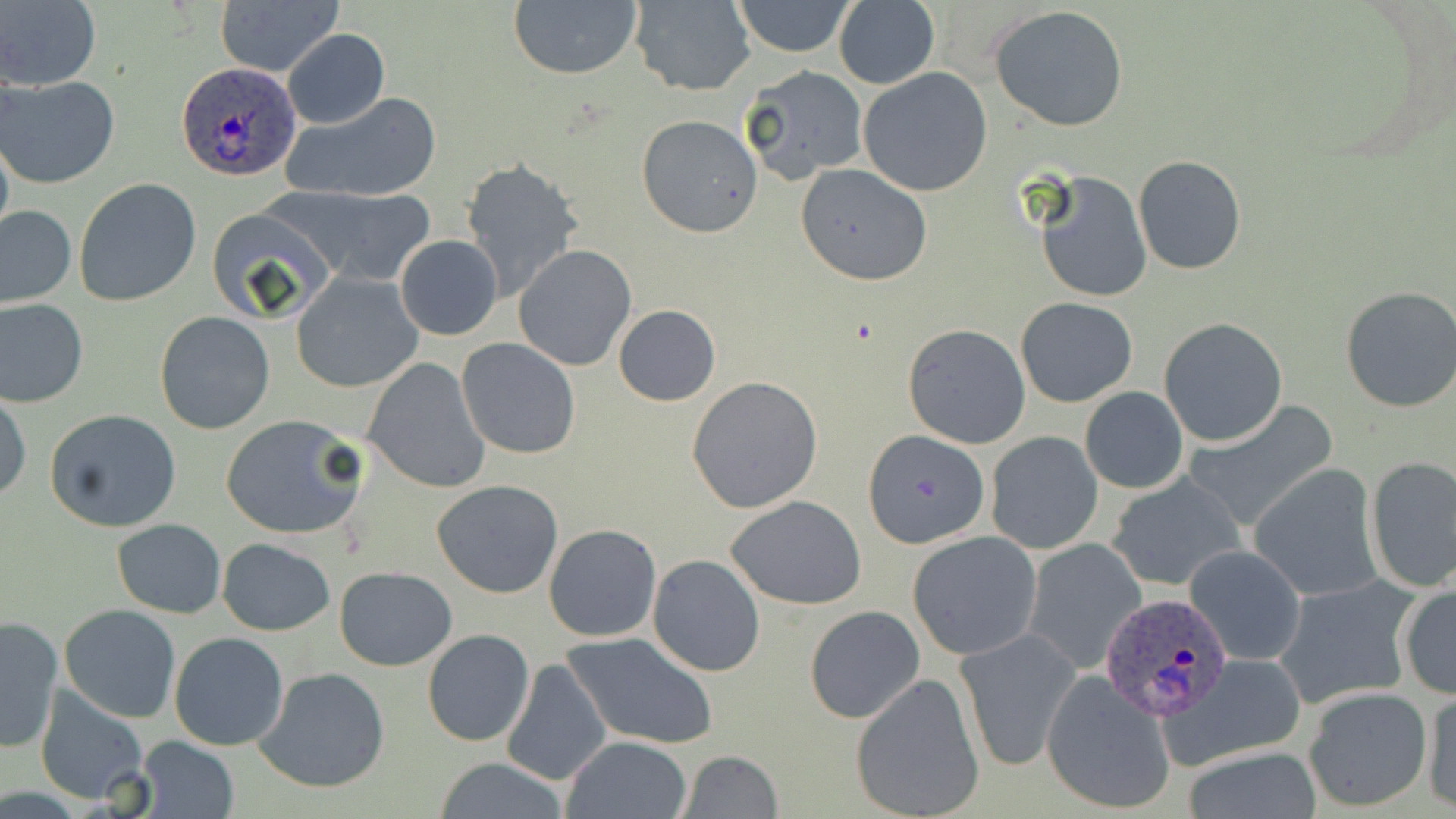
Summary:
  - Coordinate format: approximate bounding boxes as (x1,y1)-(x2,y2) corner pairs in pixels
  - Plasmodium ovale-infected red blood cell locations: (177,62)-(302,181), (1096,592)-(1232,720)
  - Uninfected red blood cell locations: (216,0)-(343,78), (507,0)-(643,81), (732,0)-(857,57), (1,1)-(101,91), (627,1)-(755,95), (834,2)-(940,88), (990,5)-(1129,131), (284,29)-(389,129), (741,64)-(870,183), (859,68)-(993,196), (2,74)-(122,188), (279,91)-(441,204), (636,116)-(763,238), (1133,155)-(1246,274), (460,159)-(583,300), (795,162)-(932,285), (1035,170)-(1152,304), (74,179)-(202,305), (283,187)-(435,285), (0,205)-(76,308), (207,207)-(340,326), (395,235)-(504,340), (514,246)-(636,371), (291,272)-(423,393), (1338,285)-(1456,414), (1015,296)-(1138,408), (0,297)-(88,408), (612,305)-(721,406), (153,311)-(275,435), (1159,317)-(1289,447), (902,323)-(1031,449), (456,338)-(581,459), (361,357)-(491,494), (686,375)-(823,513), (1081,386)-(1188,494), (0,391)-(30,506), (1184,403)-(1338,532), (46,409)-(184,533), (220,413)-(367,539), (863,431)-(989,547), (986,432)-(1102,554), (1364,455)-(1456,594), (1249,464)-(1383,603), (1105,471)-(1245,593), (430,479)-(564,599), (726,495)-(867,607), (112,519)-(225,618), (543,524)-(663,643), (906,531)-(1042,659), (217,537)-(336,635), (1021,538)-(1146,674), (1185,545)-(1306,666), (648,554)-(765,677), (333,566)-(456,670), (1271,576)-(1420,710), (1397,580)-(1456,701), (59,604)-(181,723), (804,605)-(926,725), (0,615)-(63,754), (954,626)-(1083,772), (423,630)-(533,746), (169,632)-(289,750), (563,633)-(718,750), (1162,653)-(1310,769), (500,658)-(610,788), (253,668)-(390,794), (1041,671)-(1176,816), (850,672)-(986,819), (35,684)-(152,804), (1303,688)-(1430,813), (1420,688)-(1456,813), (134,736)-(239,819), (561,736)-(692,819), (1181,745)-(1323,819), (677,750)-(783,819), (431,758)-(572,817)
  - Slide-level diagnosis: Plasmodium ovale
  - Preparation: thin blood film
  - Field of view: single
  - Image size: 1456×819 pixels
  - Stain: May-Grünwald-Giemsa
  - Modality: optical microscopy
  - Magnification: 1000x